Locate and identify every blood parasite.
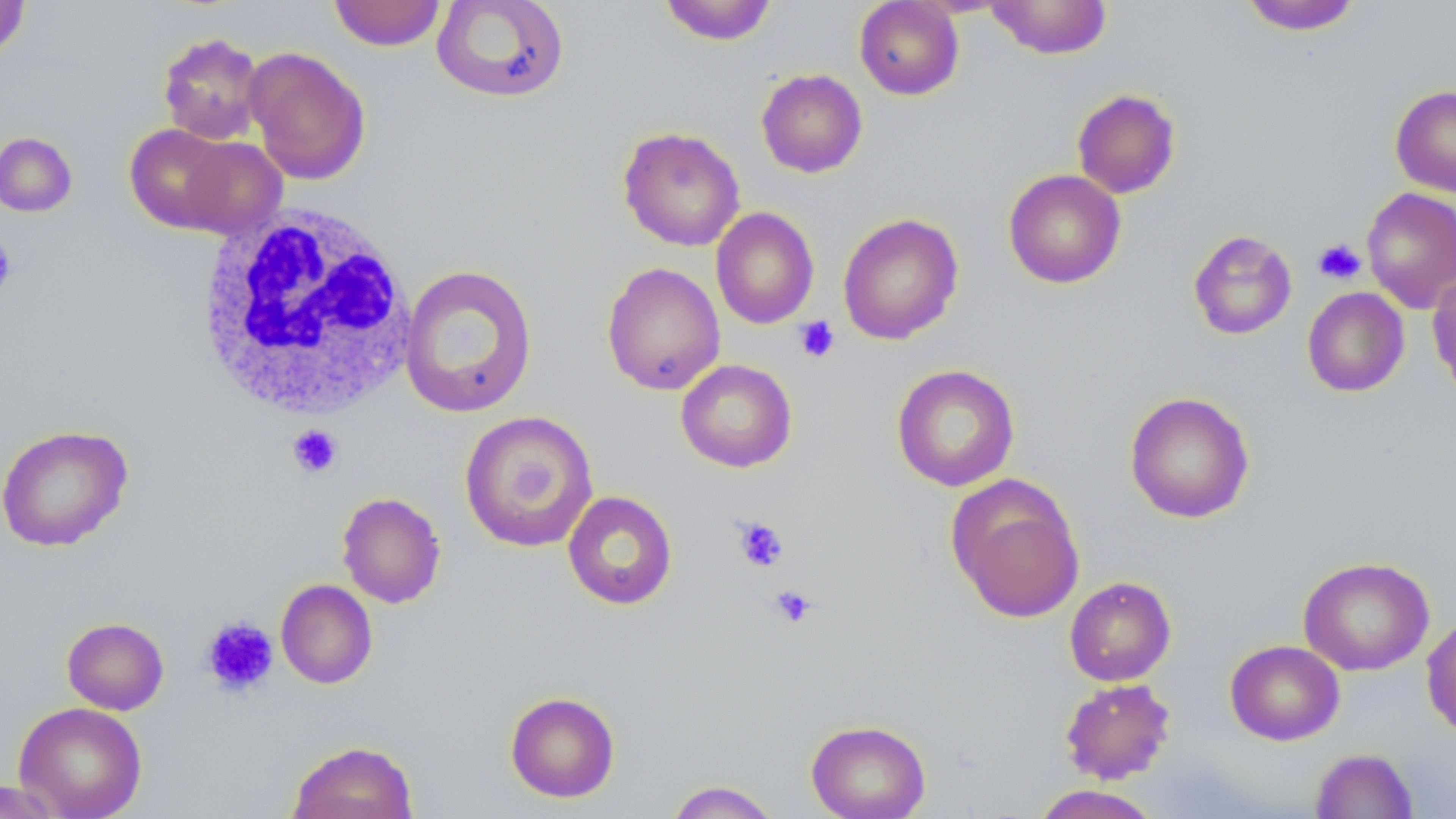
No blood parasites observed.

Approximate bounding boxes as (x1, y1, x2, y2) in pixels. Platelet locations: (0, 236, 16, 298), (1312, 238, 1366, 286), (793, 316, 840, 363), (287, 424, 343, 478), (732, 515, 789, 572), (769, 584, 817, 628), (200, 615, 279, 698). Uninfected red blood cell locations: (328, 0, 447, 51), (431, 0, 570, 103), (659, 0, 778, 45), (854, 0, 965, 100), (985, 0, 1113, 59), (0, 1, 30, 60), (1238, 1, 1363, 35), (158, 31, 266, 145), (245, 47, 371, 185), (755, 69, 868, 178), (1390, 85, 1456, 197), (1072, 88, 1181, 199), (124, 124, 239, 234), (618, 126, 745, 252), (0, 132, 78, 216), (176, 136, 287, 239), (1003, 169, 1126, 289), (1362, 187, 1456, 314), (710, 207, 819, 329), (837, 212, 964, 345), (1188, 229, 1298, 340), (602, 262, 725, 395), (399, 263, 538, 419), (1427, 270, 1456, 395), (1302, 287, 1410, 397), (676, 359, 797, 473), (891, 363, 1020, 492), (1124, 391, 1255, 523), (459, 410, 598, 552), (0, 424, 134, 551), (946, 475, 1086, 624), (562, 490, 678, 610), (337, 492, 447, 608), (1298, 556, 1434, 676), (1064, 576, 1176, 686), (276, 579, 377, 689), (1421, 612, 1456, 739), (62, 617, 169, 714), (1225, 639, 1345, 745), (1059, 678, 1176, 785), (504, 691, 620, 802), (14, 701, 147, 819), (806, 719, 931, 819), (287, 740, 418, 819), (1309, 748, 1418, 819), (0, 779, 68, 818), (665, 780, 782, 819), (1030, 784, 1164, 818). White blood cell locations: (196, 204, 416, 420). Slide-level diagnosis: negative for blood parasites. Image is 1456×819 pixels. May-Grünwald-Giemsa-stained preparation. Light microscopy. Captured at 1000x magnification. One field of a larger specimen. Thin blood smear.